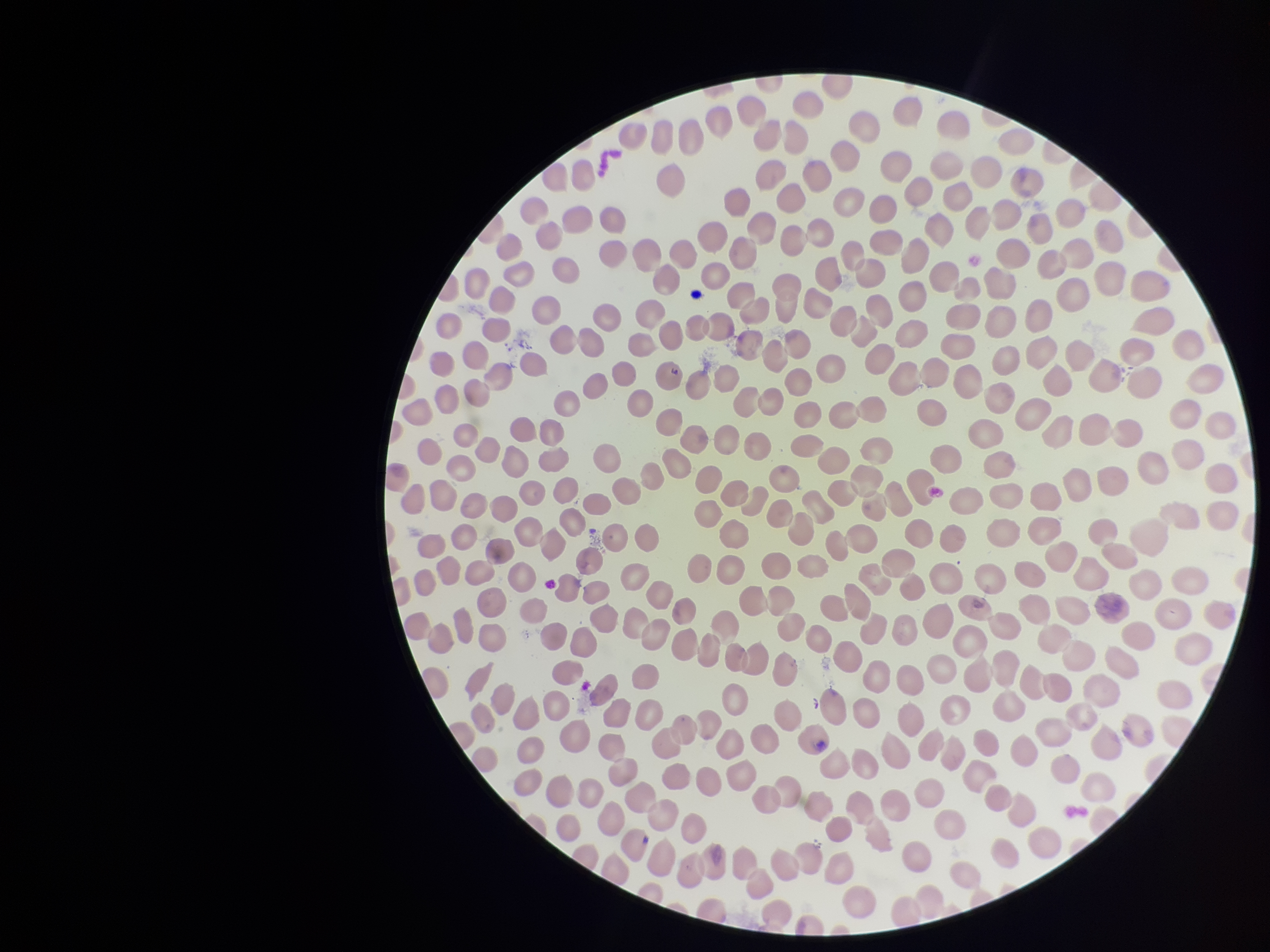
stain = Giemsa
parasitized red blood cell count = 0
preparation = thin smear
image size = 1270×952 pixels
parasitized red blood cells = none detected
field of view = single
capture = smartphone photograph through the microscope eyepiece
patient malaria status = negative
red blood cell count = 352